Assess the morphology of the erythrocytes.
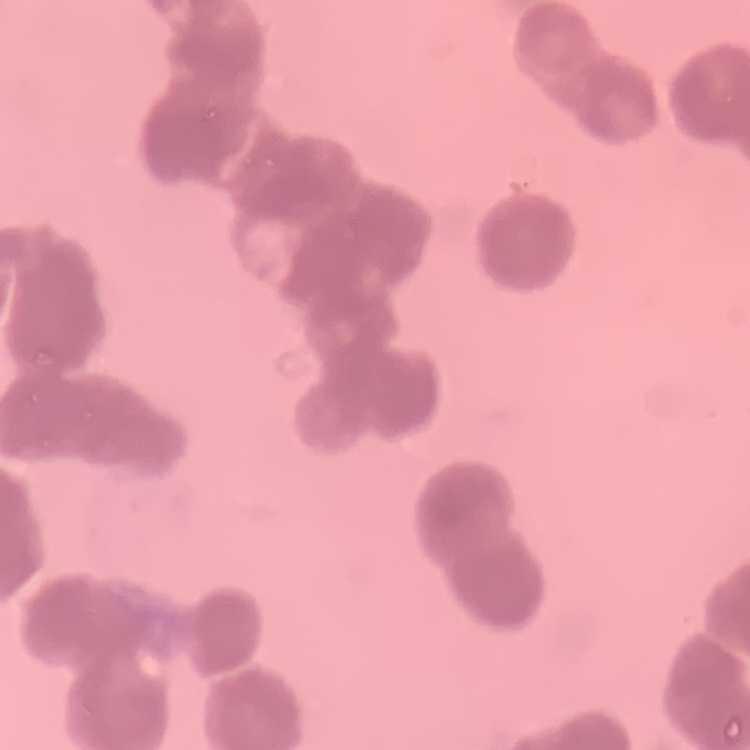
Rouleaux formation.

Summary:
  - Stain: Field's or Giemsa
  - Preparation: thin blood smear
  - Image type: square crop of a larger photomicrograph